Assess the morphology of the erythrocytes.
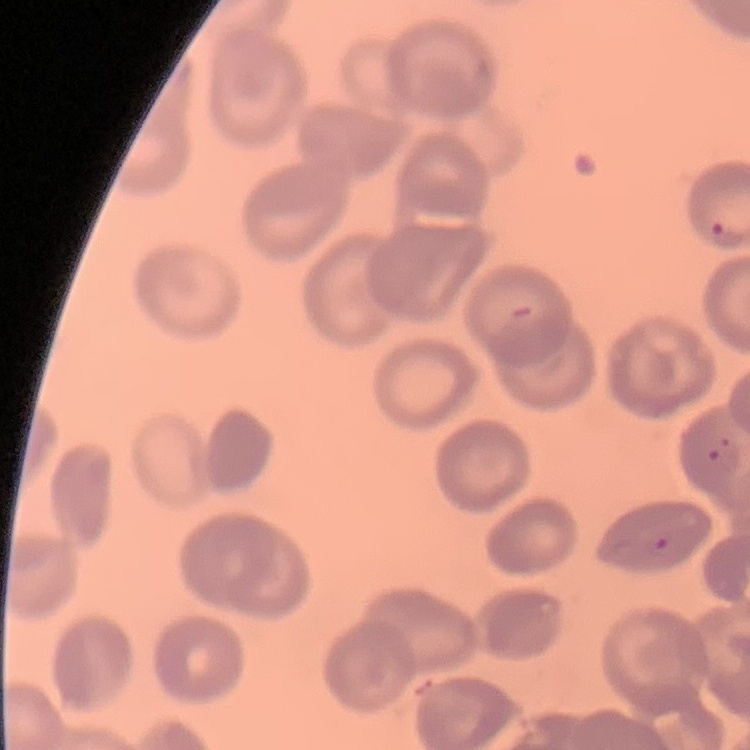

No rouleaux formation.

{
  "image_type": "square crop of a larger photomicrograph",
  "preparation": "thin peripheral smear",
  "stain": "Field's or Giemsa"
}